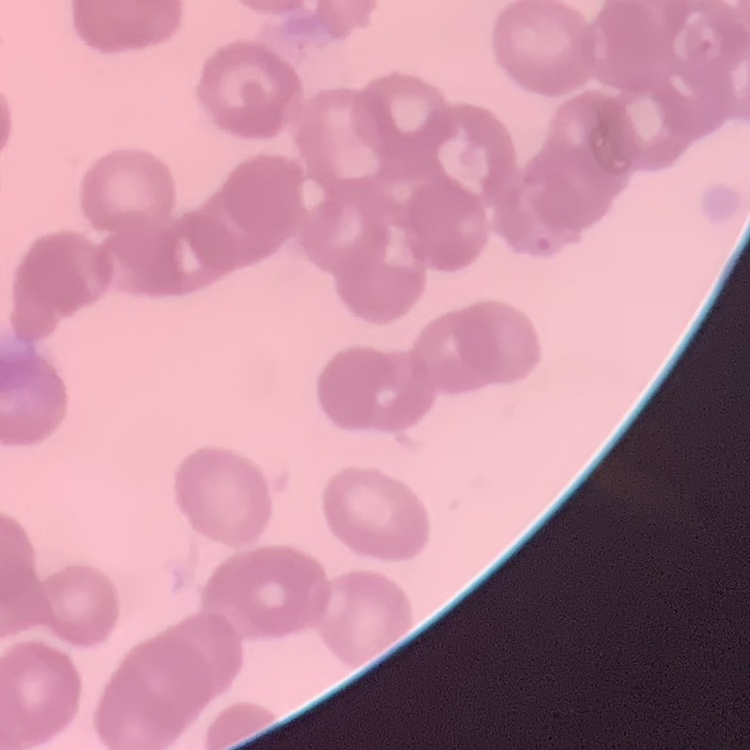

The red blood cells show rouleaux formation. Field's or Giemsa stain. Thin blood smear. One tile cut from a larger photomicrograph.